State the preparation type.
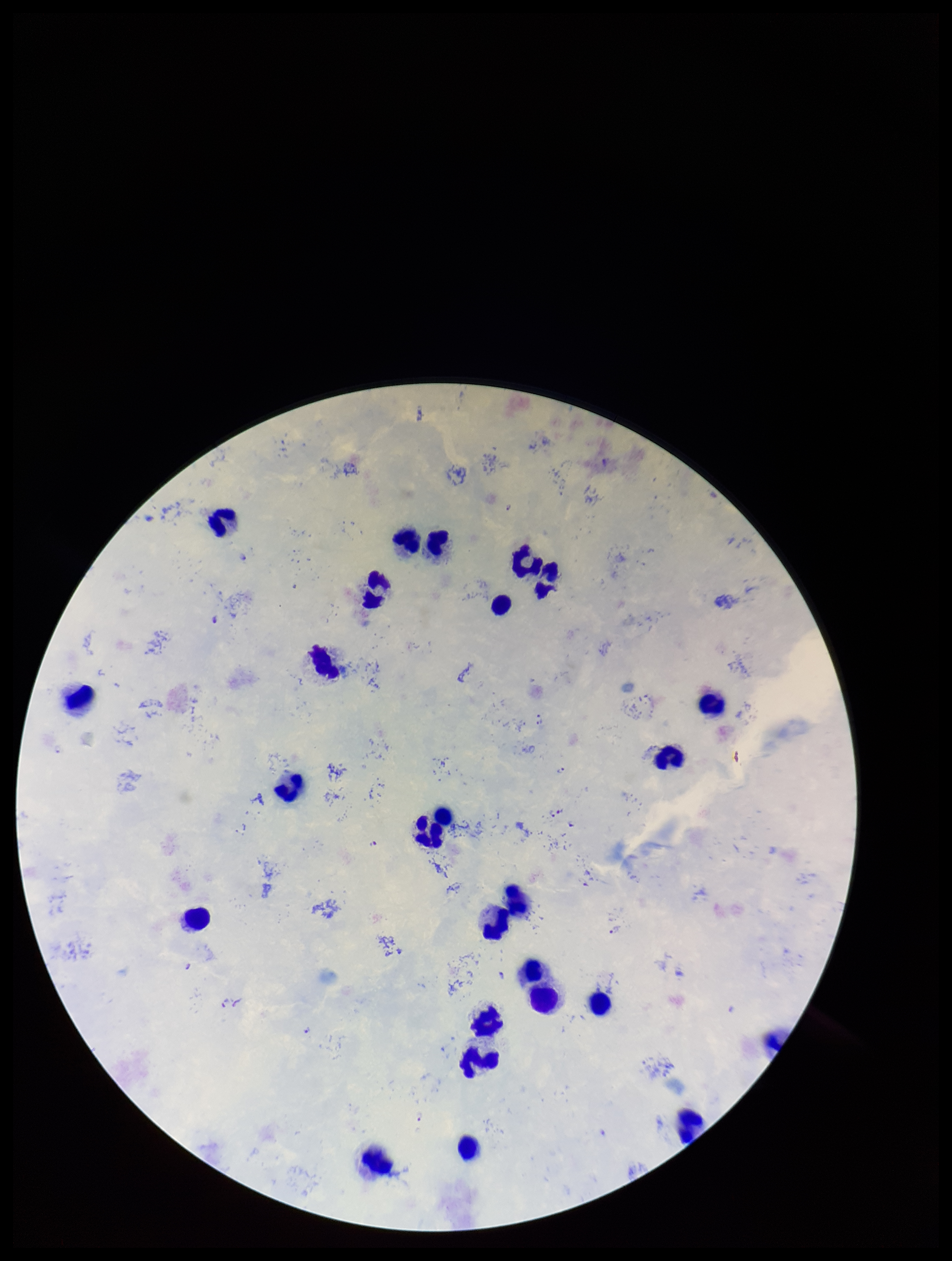

It is a thick blood smear.

Summary:
  - Image size: 952×1261 pixels
  - Plasmodium parasites: seen
  - Parasite count: 10
  - Capture: smartphone photograph through the microscope eyepiece
  - Species reported for this patient: Plasmodium falciparum
  - Stain: Giemsa
  - Leukocyte count: 25
  - Patient malaria status: infected
  - Field of view: one from this slide